Report the malaria status.
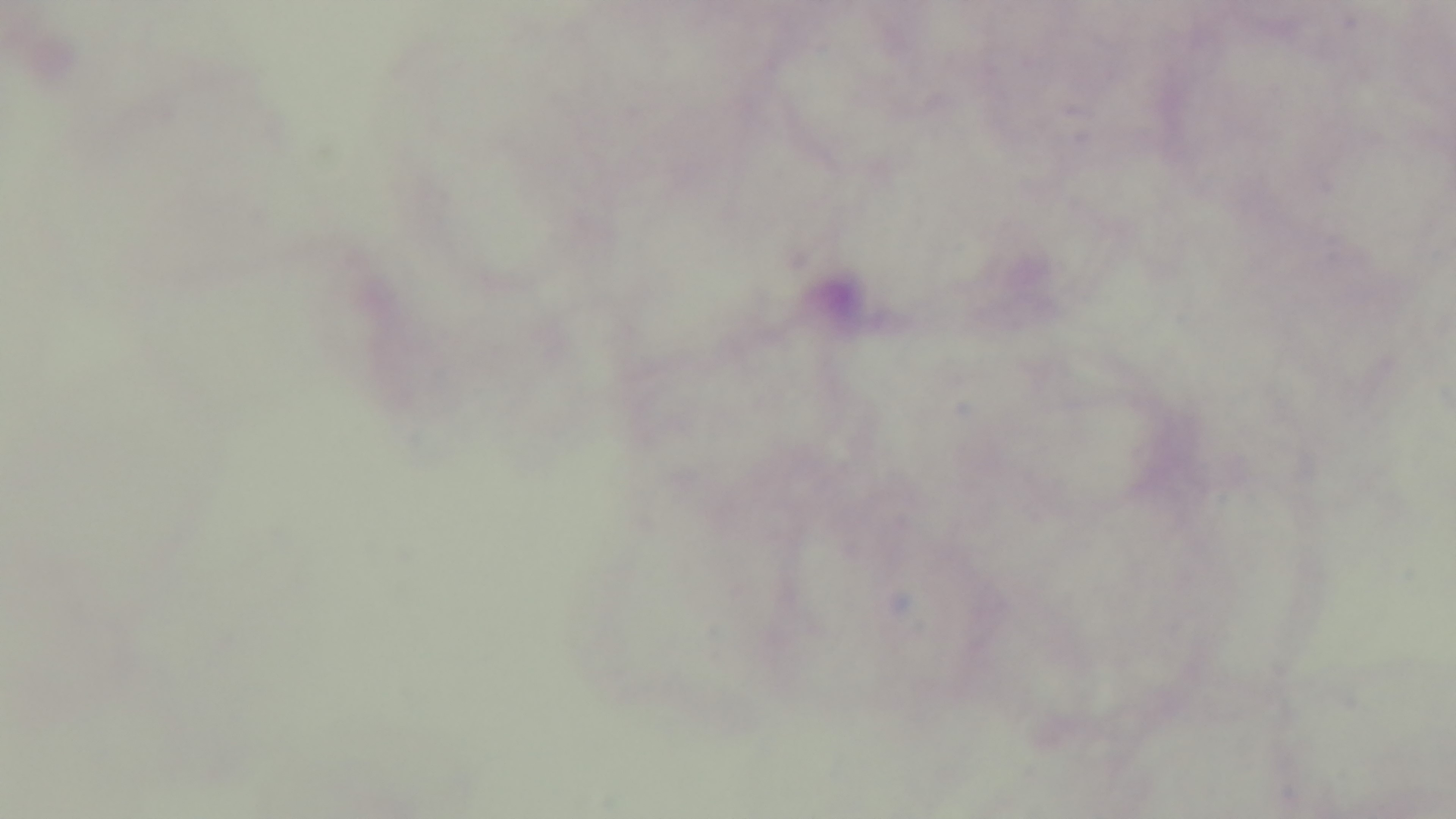
Negative.

Summary:
  - Field of view: one from the slide
  - Capture: mounted 4K digital camera
  - Modality: light microscopy
  - Preparation: thick
  - Stain: Giemsa
  - Objective: 100x oil immersion